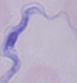
Photomicrograph. A trypanosome is shown. Captured at 1000x magnification.